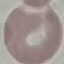

malaria status = uninfected
image type = automatically extracted cell patch, resized to 64 × 64 pixels
preparation = thin blood film
stain = Giemsa
capture = smartphone camera at the microscope eyepiece